Report the malaria status of this cell.
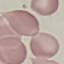

It is uninfected.

Summary:
  - Stain: Giemsa
  - Image type: cell patch, automatically extracted from a larger field of view and resized to 64 × 64 pixels
  - Capture: smartphone camera at the microscope eyepiece
  - Preparation: thin smear